Report the malaria status of this cell.
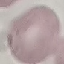

It is uninfected.

Cell patch, automatically extracted from a larger field of view and resized to 64 × 64 pixels. Acquired by smartphone through the microscope eyepiece. Giemsa-stained preparation. Thin blood film.